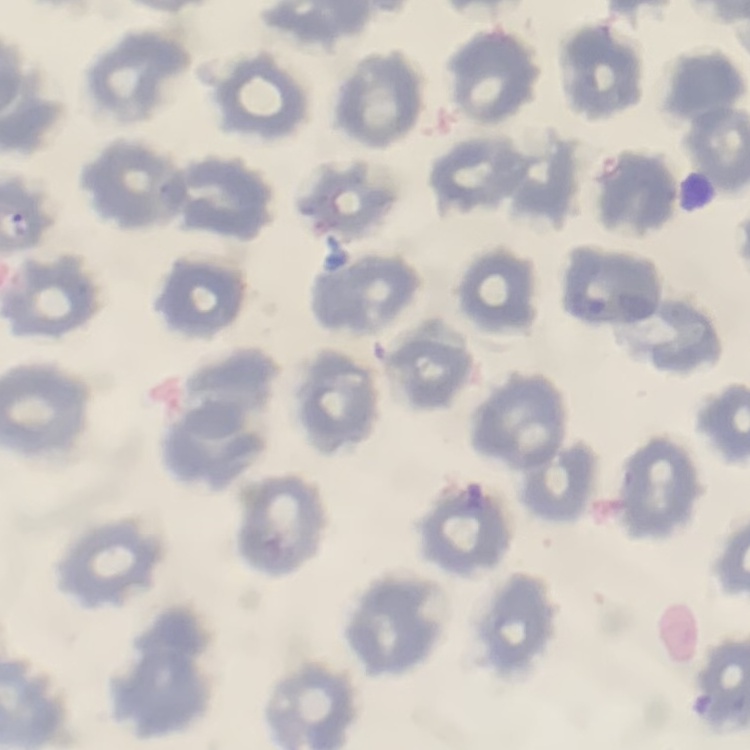

Summary:
  - Erythrocyte morphology: no rouleaux formation
  - Preparation: thin blood smear
  - Image type: square crop of a larger photomicrograph
  - Stain: Field's or Giemsa